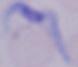

{
  "modality": "micrograph",
  "magnification": "1000x",
  "identification": "trypanosome"
}